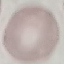

result: no malaria parasites seen
capture: smartphone through the microscope eyepiece
stain: Giemsa
preparation: thin blood smear
image_type: cell patch, automatically extracted from a larger field of view and resized to 64 × 64 pixels